Locate every uninfected red blood cell.
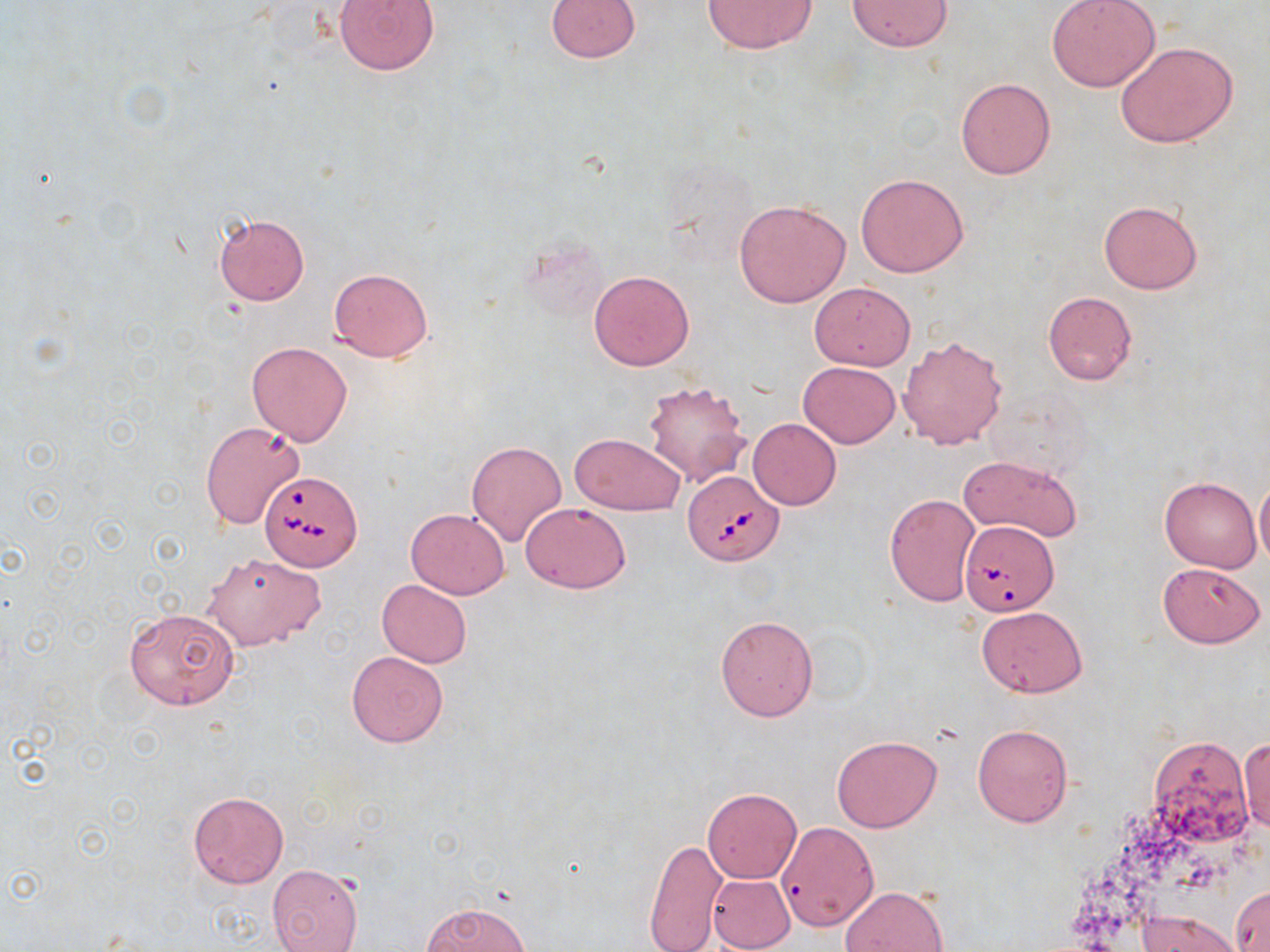
Approximate bounding boxes as (x1,y1)-(x2,y2) corner pairs in pixels.
Uninfected red blood cells: (334,0)-(441,75), (701,0)-(817,53), (1047,0)-(1160,91), (545,1)-(641,62), (846,1)-(954,52), (1114,40)-(1238,148), (956,77)-(1056,180), (856,173)-(969,278), (733,199)-(851,307), (1098,200)-(1203,294), (213,212)-(310,305), (329,268)-(432,361), (589,269)-(695,371), (809,282)-(916,370), (1043,291)-(1138,385), (897,334)-(1007,449), (247,341)-(353,445), (798,361)-(900,448), (642,380)-(752,488), (748,418)-(841,510), (200,421)-(306,530), (570,433)-(685,514), (466,440)-(567,547), (958,455)-(1083,541), (1160,475)-(1260,573), (1254,478)-(1270,569), (885,493)-(980,606), (520,501)-(632,594), (405,507)-(510,598), (202,553)-(326,651), (1156,562)-(1267,648), (377,580)-(472,668), (978,606)-(1087,697), (124,608)-(239,709), (715,615)-(818,721), (346,651)-(447,746), (972,724)-(1072,826), (831,735)-(941,832), (1148,736)-(1252,844), (1239,738)-(1270,834), (703,788)-(801,884), (189,791)-(288,888), (776,821)-(879,930), (644,837)-(727,952), (267,863)-(363,950), (707,873)-(797,952), (1231,884)-(1269,951), (841,886)-(949,952), (423,901)-(529,952), (1137,909)-(1241,952).

Babesia divergens-infected red blood cell locations: (683,469)-(785,566), (259,470)-(361,571), (959,520)-(1056,613). Slide-level diagnosis: Babesia divergens. Light microscopy. Single field of view. Image is 1270×952 pixels. Thin blood film. Captured at 1000x magnification. May-Grünwald-Giemsa stain.